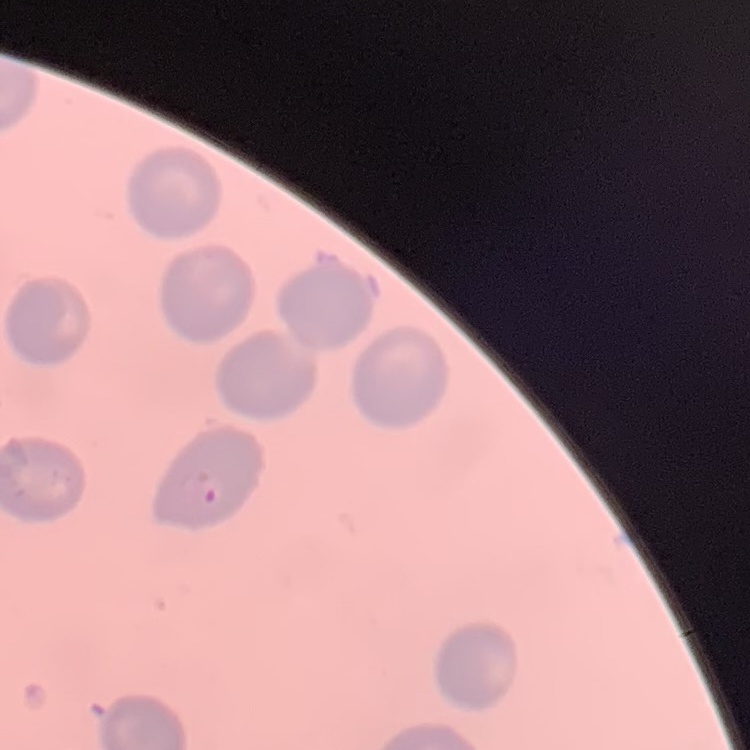
{
  "erythrocyte_morphology": "no rouleaux formation",
  "image_type": "square crop of a larger photomicrograph",
  "stain": "Field's or Giemsa",
  "preparation": "thin blood smear"
}